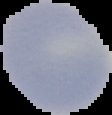
Summary:
  - Image size: 112×115 pixels
  - Result: no malaria parasites detected
  - Preparation: thin blood smear
  - Image type: segmented cell region with the area outside set to black